Mark where leukocytes are.
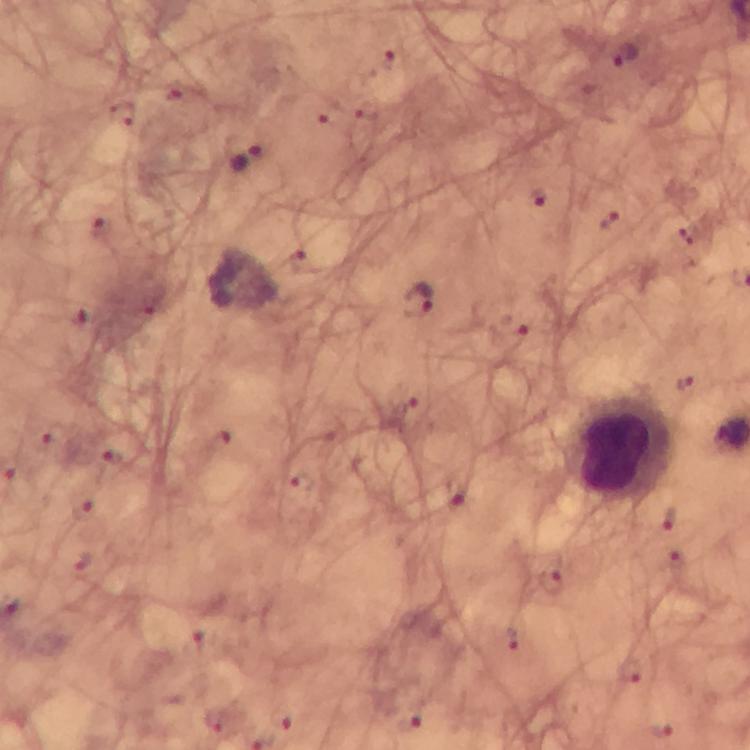

Approximate object centers, in pixels from the top-left corner.
Leukocytes: (x=624, y=448).

Malaria parasite locations: (x=627, y=55), (x=249, y=159), (x=542, y=196), (x=611, y=220), (x=101, y=229), (x=420, y=299), (x=73, y=314), (x=509, y=329), (x=404, y=397), (x=53, y=438), (x=109, y=456), (x=299, y=482), (x=458, y=491), (x=84, y=507), (x=668, y=519), (x=549, y=586), (x=514, y=637), (x=632, y=671), (x=283, y=716), (x=406, y=721), (x=661, y=729). Photographed through the microscope with a smartphone camera. Image is 750×750 pixels. From a diagnostic examination for malaria. Thick blood film. Giemsa-stained preparation. Immersion oil applied. 100x magnification. Cropped region of a single field of view.